Classify the preparation.
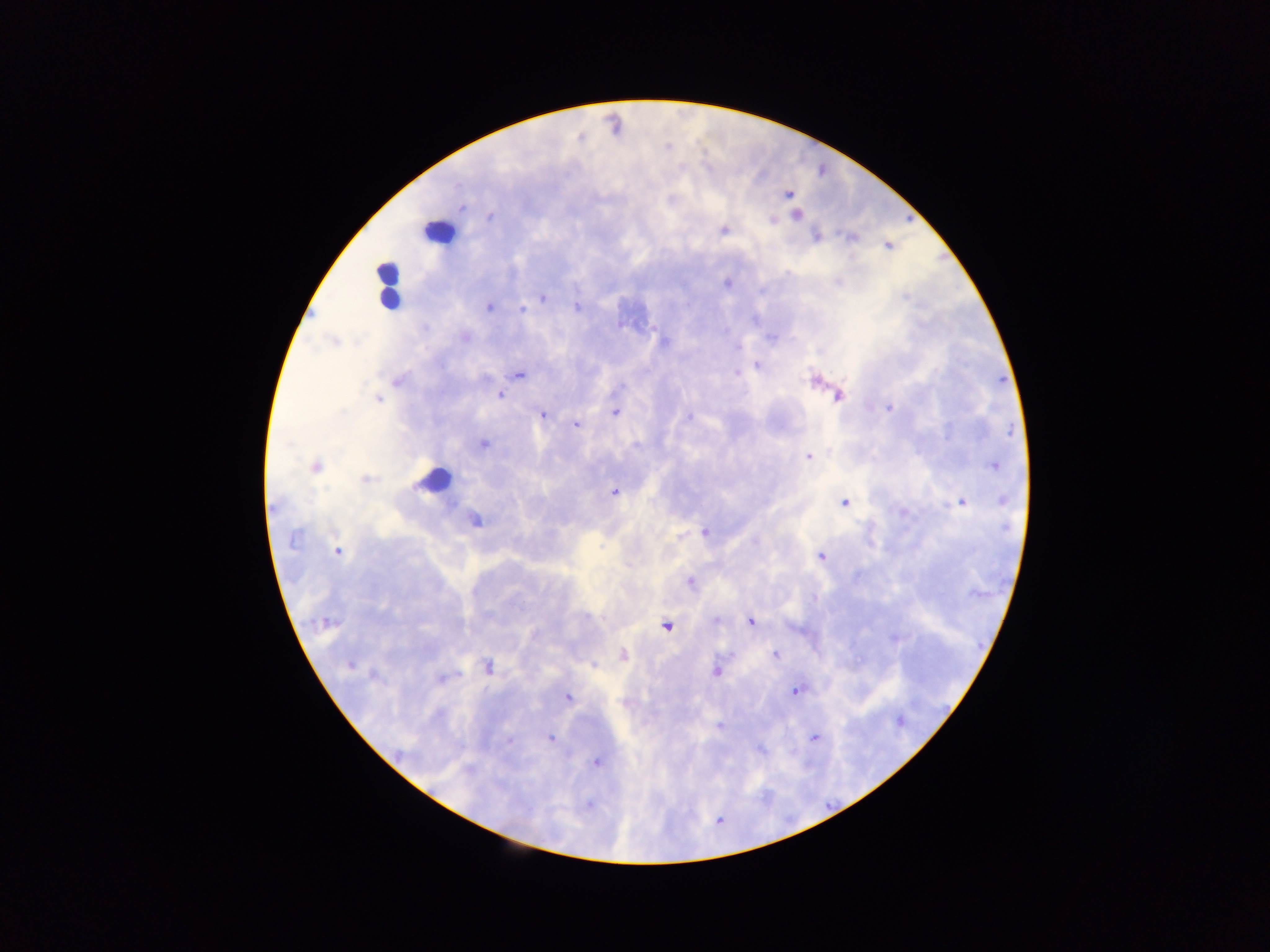
Thick blood film.

Approximate centers as [x, y] in pixels.
Summary:
  - Plasmodium parasite locations: [788, 194], [796, 215], [490, 216], [773, 218], [724, 230], [816, 236], [887, 245], [726, 282], [542, 297], [489, 306], [576, 306], [522, 309], [334, 342], [758, 365], [518, 374], [813, 379], [499, 394], [838, 396], [377, 399], [888, 407], [615, 411], [542, 415], [575, 423], [483, 444], [808, 455], [993, 464], [315, 466], [366, 480], [614, 492], [961, 501], [844, 502], [474, 519], [705, 531], [336, 551], [822, 557], [690, 583], [716, 620], [751, 621], [327, 623], [666, 625], [623, 655], [775, 655], [350, 664], [593, 665], [487, 667], [716, 670], [442, 677], [795, 690], [567, 696], [551, 738], [813, 738], [509, 740], [596, 761], [588, 804], [718, 819]
  - Leukocyte locations: [438, 233], [388, 284], [434, 480]
  - Capture: mobile-phone photograph through a microscope
  - Field of view: single
  - Image size: 1270×952 pixels
  - Country: Ghana